Locate every blood parasite and identify its species.
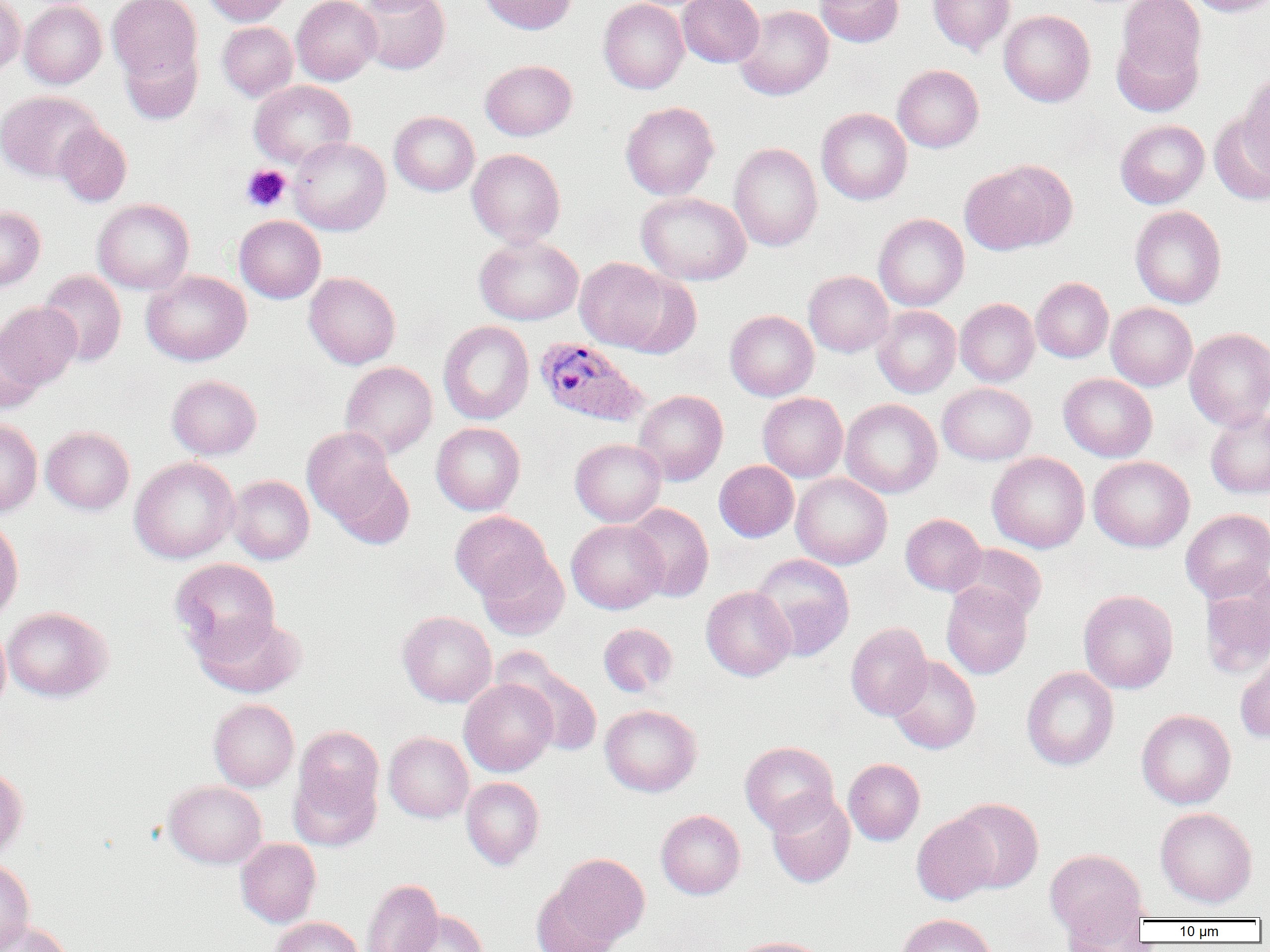
Approximate bounding boxes as (x1, y1, x2, y2) in pixels.
Plasmodium ovale-infected red blood cells: (534, 338, 648, 427).
No Plasmodium falciparum, Plasmodium malariae, Plasmodium vivax, Babesia divergens, or Trypanosoma brucei observed.

Summary:
  - Uninfected red blood cell locations: (0, 0, 26, 75), (107, 0, 202, 82), (203, 0, 292, 26), (292, 0, 381, 85), (356, 0, 446, 15), (357, 0, 449, 75), (478, 0, 577, 34), (599, 0, 689, 94), (677, 0, 764, 67), (815, 0, 904, 47), (928, 0, 1015, 55), (1115, 0, 1205, 80), (1187, 0, 1270, 16), (19, 1, 106, 88), (735, 5, 833, 100), (999, 10, 1095, 107), (217, 22, 298, 101), (1111, 30, 1203, 116), (121, 42, 202, 124), (480, 59, 577, 140), (892, 64, 983, 152), (1239, 71, 1270, 174), (249, 80, 355, 167), (0, 90, 103, 182), (621, 101, 719, 200), (817, 108, 912, 205), (389, 111, 479, 196), (1210, 113, 1270, 206), (1115, 119, 1209, 208), (54, 122, 132, 207), (289, 137, 390, 236), (729, 143, 822, 251), (467, 149, 566, 247), (959, 160, 1076, 255), (636, 192, 751, 285), (92, 199, 194, 294), (0, 206, 45, 291), (1130, 206, 1226, 308), (873, 213, 969, 311), (234, 215, 326, 303), (474, 235, 583, 325), (574, 257, 673, 352), (38, 270, 126, 367), (141, 270, 251, 365), (804, 270, 893, 357), (615, 271, 702, 358), (304, 272, 401, 369), (1032, 277, 1113, 362), (955, 298, 1039, 386), (0, 302, 82, 391), (1106, 302, 1197, 390), (873, 306, 961, 397), (725, 310, 818, 401), (438, 321, 534, 424), (1185, 328, 1270, 429), (0, 333, 43, 414), (340, 361, 438, 458), (1059, 373, 1157, 462), (167, 375, 262, 459), (937, 383, 1036, 464), (633, 390, 728, 485), (758, 392, 848, 482), (840, 399, 941, 498), (1206, 408, 1270, 498), (0, 419, 42, 516), (431, 422, 525, 515), (41, 426, 135, 514), (302, 427, 398, 525), (570, 438, 666, 527), (988, 452, 1090, 553), (321, 453, 415, 550), (1088, 456, 1194, 552), (129, 457, 240, 563), (714, 460, 799, 542), (791, 473, 892, 569), (227, 475, 314, 564), (625, 503, 714, 601), (1181, 508, 1270, 602), (450, 511, 550, 600), (900, 513, 986, 595), (0, 515, 23, 623), (566, 520, 666, 614), (952, 544, 1047, 623), (477, 548, 569, 640), (751, 553, 855, 660), (170, 558, 281, 660), (1200, 569, 1270, 678), (941, 583, 1032, 679), (701, 586, 795, 681), (1078, 589, 1178, 694), (2, 607, 113, 702), (398, 611, 497, 707), (194, 612, 307, 698), (0, 620, 10, 716), (598, 623, 678, 697), (845, 623, 933, 720), (496, 649, 603, 756), (1235, 651, 1270, 743), (886, 656, 981, 754), (1021, 667, 1119, 770), (459, 679, 557, 776), (208, 699, 299, 791), (600, 704, 701, 797), (1137, 709, 1236, 809), (294, 725, 384, 815), (384, 732, 473, 822), (740, 741, 839, 834), (844, 758, 925, 845), (0, 764, 28, 860), (289, 766, 381, 851), (461, 777, 544, 869), (163, 780, 267, 868), (767, 792, 855, 887), (949, 798, 1043, 893), (1155, 808, 1257, 907), (656, 809, 745, 899), (911, 813, 999, 905), (236, 839, 321, 927), (1045, 848, 1148, 942), (549, 852, 650, 948), (0, 858, 35, 952), (361, 878, 443, 952), (532, 886, 621, 952), (1062, 903, 1148, 951), (400, 910, 488, 952), (896, 913, 998, 952), (269, 916, 364, 952), (0, 919, 73, 952), (730, 936, 829, 952)
  - Platelet locations: (241, 165, 291, 212)
  - Slide-level diagnosis: Plasmodium ovale
  - Magnification: 1000x
  - Field of view: single
  - Modality: light microscopy
  - Preparation: thin blood film
  - Image size: 1270×952 pixels